Identify the blood parasite species.
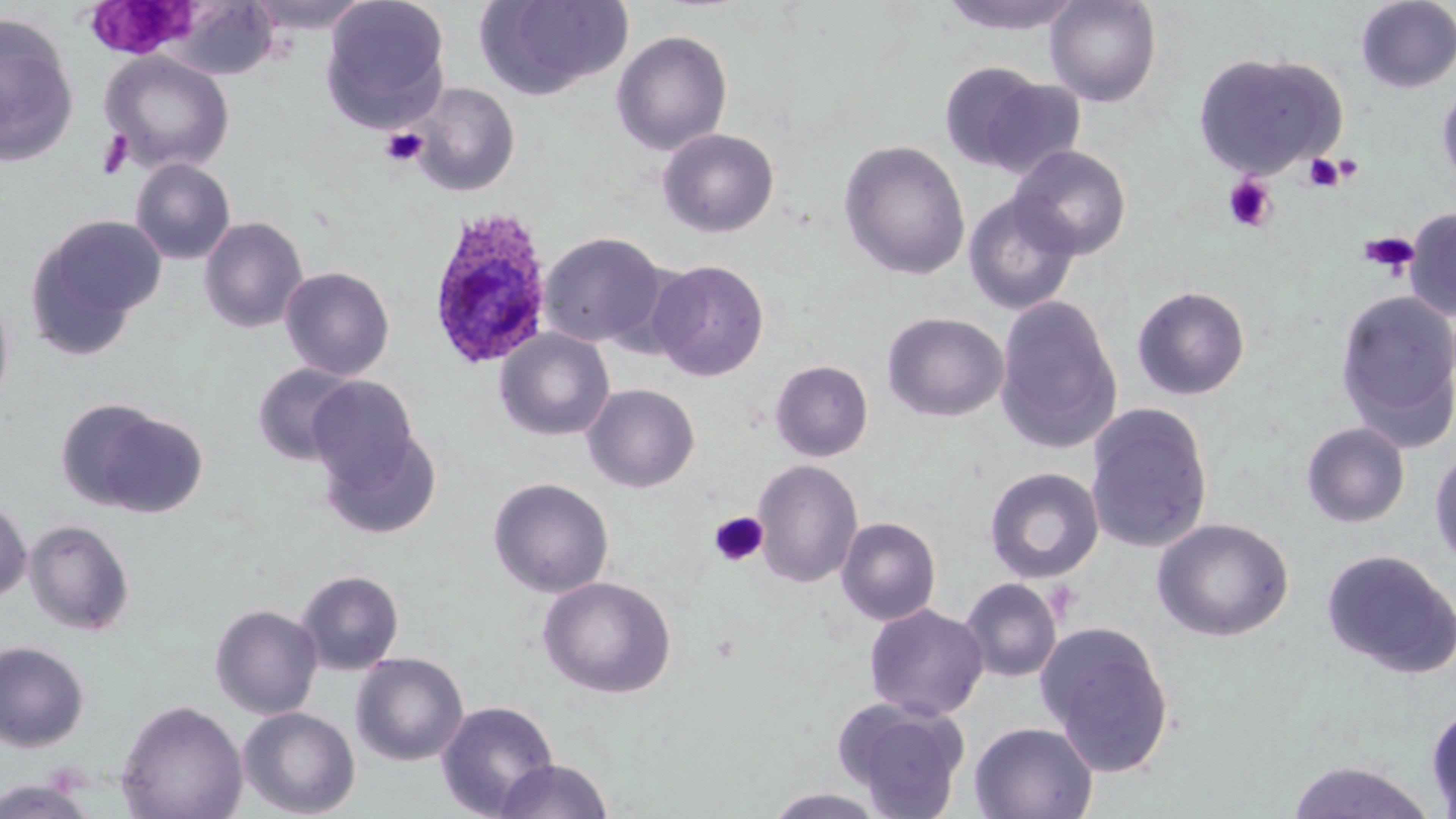

Plasmodium ovale.

Approximate bounding boxes as [x1, y1, x2, y2] in pixels. Plasmodium ovale-infected red blood cell locations: [426, 207, 554, 370]. Uninfected red blood cell locations: [242, 0, 374, 33], [320, 0, 451, 131], [475, 0, 634, 99], [937, 0, 1087, 36], [1045, 0, 1162, 107], [167, 1, 280, 80], [1355, 1, 1456, 93], [0, 16, 79, 165], [611, 30, 732, 156], [99, 51, 235, 173], [1192, 51, 1347, 179], [939, 62, 1047, 171], [975, 77, 1087, 179], [1437, 78, 1456, 193], [410, 82, 520, 197], [656, 128, 780, 238], [838, 140, 971, 281], [1009, 145, 1132, 260], [129, 158, 236, 265], [962, 192, 1081, 316], [1405, 207, 1456, 321], [26, 214, 165, 354], [198, 216, 308, 333], [538, 231, 668, 348], [648, 259, 769, 381], [279, 266, 395, 380], [1131, 284, 1251, 400], [0, 285, 14, 418], [1334, 290, 1456, 448], [993, 295, 1123, 455], [882, 312, 1009, 422], [494, 328, 615, 441], [770, 359, 873, 462], [251, 363, 360, 465], [307, 375, 421, 491], [581, 383, 701, 493], [1085, 402, 1214, 554], [74, 405, 209, 517], [317, 420, 443, 541], [1301, 422, 1411, 528], [1429, 445, 1456, 571], [752, 459, 864, 588], [983, 466, 1105, 583], [487, 477, 614, 598], [0, 496, 32, 604], [836, 516, 941, 626], [1151, 517, 1294, 642], [24, 519, 135, 636], [1320, 549, 1456, 678], [295, 569, 404, 675], [537, 575, 676, 699], [959, 578, 1062, 683], [209, 603, 323, 719], [864, 603, 989, 721], [1036, 621, 1175, 778], [0, 641, 89, 753], [351, 652, 469, 765], [116, 699, 248, 819], [835, 699, 971, 817], [436, 700, 559, 818], [1425, 703, 1456, 817], [238, 706, 361, 818], [968, 721, 1098, 819], [494, 758, 616, 819], [1285, 760, 1440, 819], [0, 777, 98, 818], [761, 787, 890, 818]. Platelet locations: [87, 3, 197, 57], [381, 127, 428, 168], [96, 129, 134, 179], [1304, 153, 1346, 193], [1222, 175, 1278, 232], [1360, 231, 1419, 276], [709, 511, 769, 567]. 1000x magnification. Thin blood smear. Image is 1456×819 pixels. Single field of view. Optical microscopy. May-Grünwald-Giemsa stain.